State the blood parasite species.
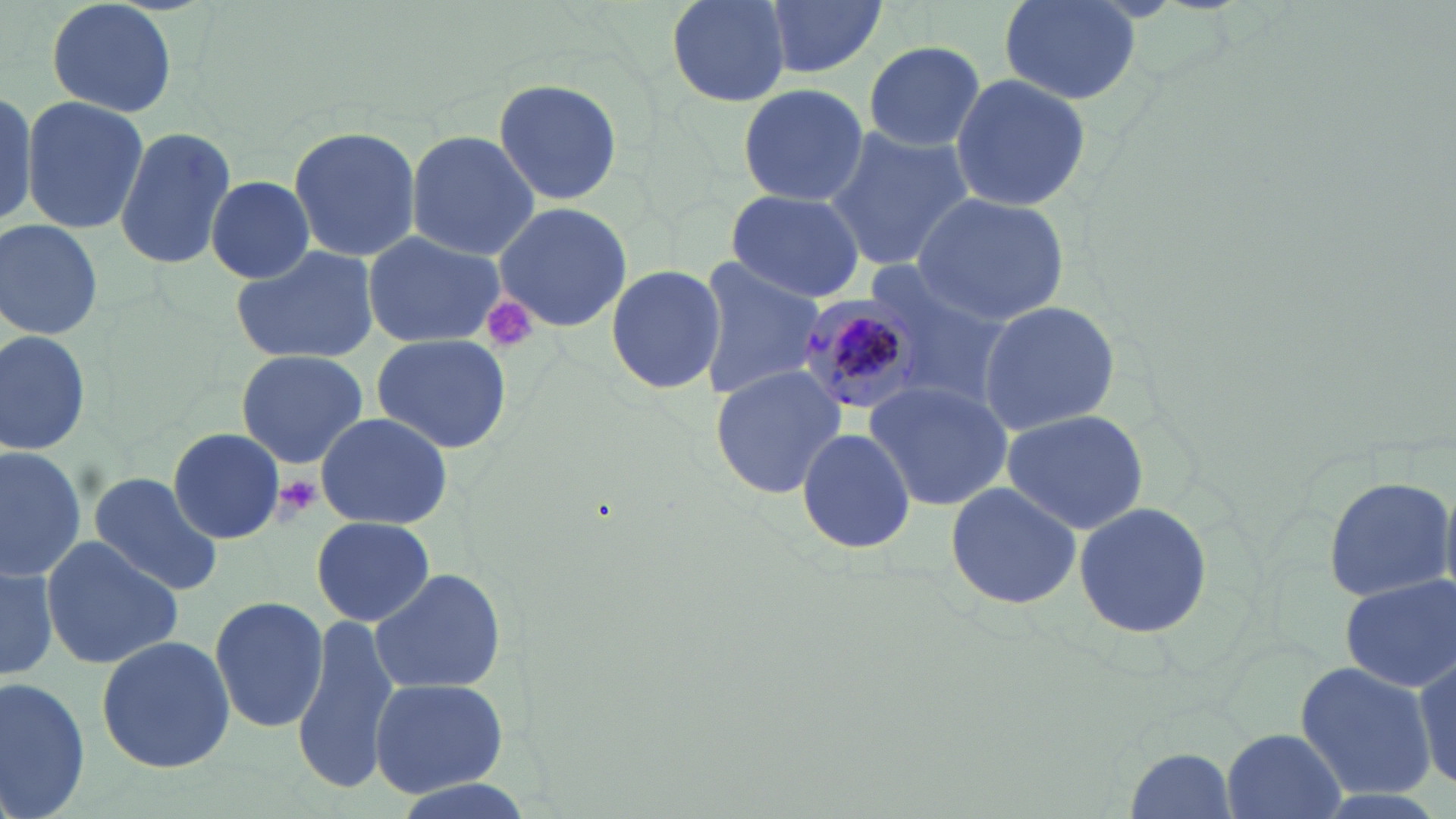

Plasmodium malariae.

Summary:
  - Coordinate format: approximate bounding boxes as named x1/y1/x2/y2 corners in pixels
  - Plasmodium malariae-infected red blood cell locations: (x1=795, y1=289, x2=932, y2=415)
  - Uninfected red blood cell locations: (x1=45, y1=0, x2=179, y2=119), (x1=662, y1=0, x2=792, y2=105), (x1=762, y1=0, x2=886, y2=80), (x1=998, y1=0, x2=1142, y2=103), (x1=862, y1=39, x2=986, y2=153), (x1=948, y1=73, x2=1093, y2=212), (x1=491, y1=77, x2=624, y2=207), (x1=736, y1=84, x2=869, y2=208), (x1=0, y1=87, x2=36, y2=234), (x1=20, y1=95, x2=150, y2=234), (x1=288, y1=124, x2=422, y2=261), (x1=114, y1=125, x2=239, y2=269), (x1=824, y1=126, x2=973, y2=272), (x1=405, y1=131, x2=542, y2=261), (x1=205, y1=175, x2=318, y2=282), (x1=724, y1=189, x2=867, y2=303), (x1=911, y1=192, x2=1071, y2=323), (x1=493, y1=202, x2=633, y2=330), (x1=0, y1=219, x2=103, y2=339), (x1=360, y1=229, x2=509, y2=351), (x1=230, y1=242, x2=379, y2=364), (x1=693, y1=259, x2=824, y2=400), (x1=605, y1=263, x2=727, y2=395), (x1=977, y1=299, x2=1120, y2=435), (x1=0, y1=329, x2=91, y2=457), (x1=370, y1=334, x2=515, y2=454), (x1=234, y1=349, x2=369, y2=466), (x1=709, y1=365, x2=845, y2=500), (x1=863, y1=380, x2=1012, y2=510), (x1=1000, y1=408, x2=1149, y2=536), (x1=314, y1=411, x2=453, y2=530), (x1=795, y1=426, x2=917, y2=557), (x1=169, y1=427, x2=285, y2=542), (x1=0, y1=445, x2=85, y2=578), (x1=114, y1=445, x2=278, y2=574), (x1=86, y1=472, x2=226, y2=594), (x1=1322, y1=475, x2=1454, y2=604), (x1=943, y1=482, x2=1083, y2=611), (x1=1071, y1=498, x2=1217, y2=641), (x1=310, y1=515, x2=437, y2=627), (x1=40, y1=534, x2=184, y2=670), (x1=0, y1=557, x2=59, y2=683), (x1=370, y1=567, x2=506, y2=695), (x1=1340, y1=575, x2=1455, y2=692), (x1=208, y1=595, x2=329, y2=731), (x1=292, y1=613, x2=399, y2=794), (x1=96, y1=633, x2=237, y2=772), (x1=1413, y1=650, x2=1454, y2=792), (x1=1295, y1=661, x2=1433, y2=802), (x1=0, y1=673, x2=91, y2=819), (x1=367, y1=676, x2=513, y2=797), (x1=1222, y1=728, x2=1346, y2=819), (x1=1122, y1=744, x2=1241, y2=819)
  - Platelet locations: (x1=479, y1=295, x2=541, y2=354), (x1=270, y1=475, x2=323, y2=520)
  - Magnification: 1000x
  - Stain: May-Grünwald-Giemsa
  - Preparation: thin blood smear
  - Modality: light microscopy
  - Image size: 1456×819 pixels
  - Field of view: one of a larger specimen